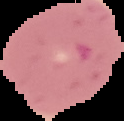

result = negative for Plasmodium parasites
preparation = thin blood smear
image type = segmented cell region on a black background
image size = 124×121 pixels